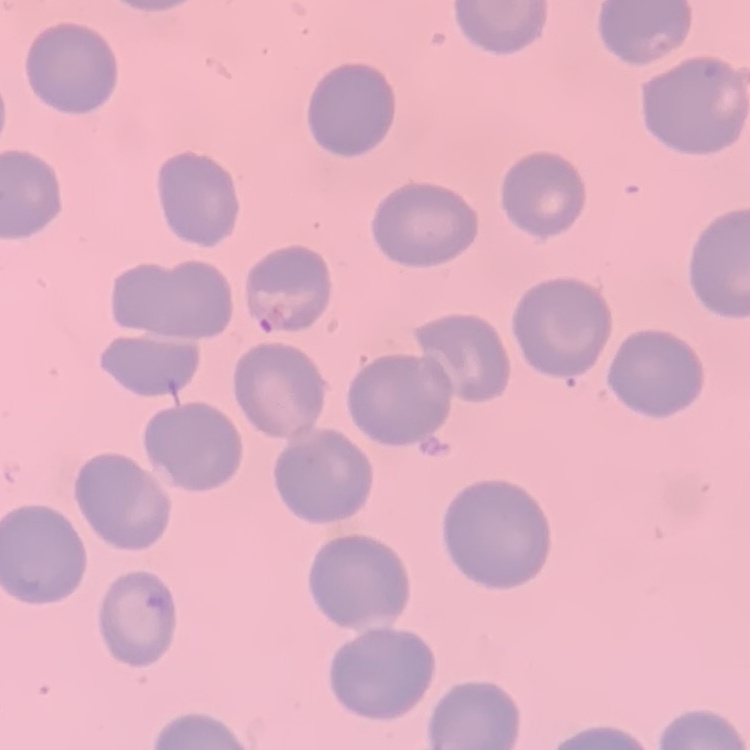
The red blood cells exhibit no rouleaux formation. Thin blood smear. Stained with either Field's or Giemsa. One tile cut from a larger photomicrograph.